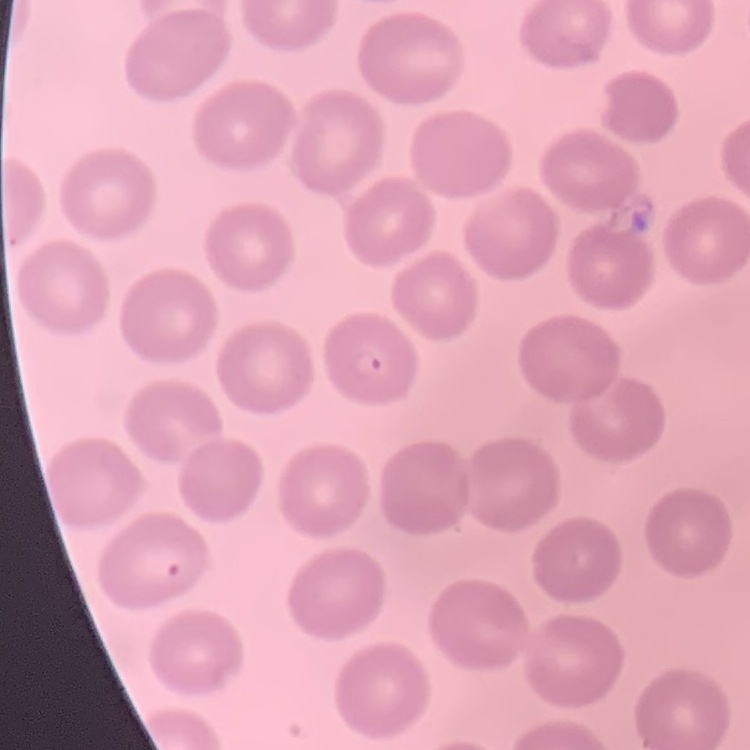
Summary:
  - Red blood cell morphology: no rouleaux formation
  - Preparation: thin blood smear
  - Image type: square crop of a larger photomicrograph
  - Stain: Field's or Giemsa